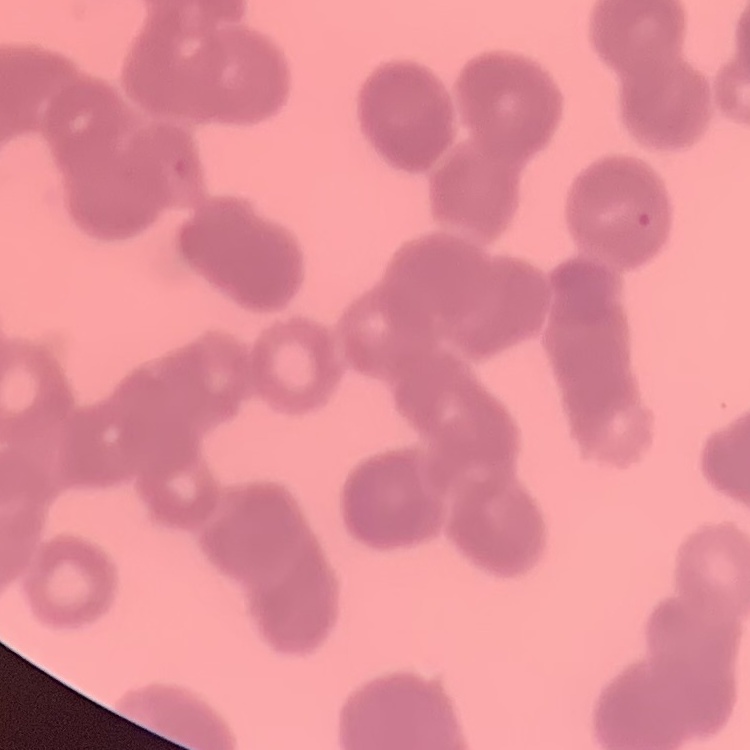
The erythrocytes show rouleaux formation. One tile cut from a larger photomicrograph. Field's or Giemsa stain. Thin blood film.